State which cell type is depicted.
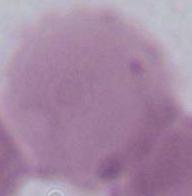

An erythrocyte.

Captured at 1000x magnification. Photomicrograph.